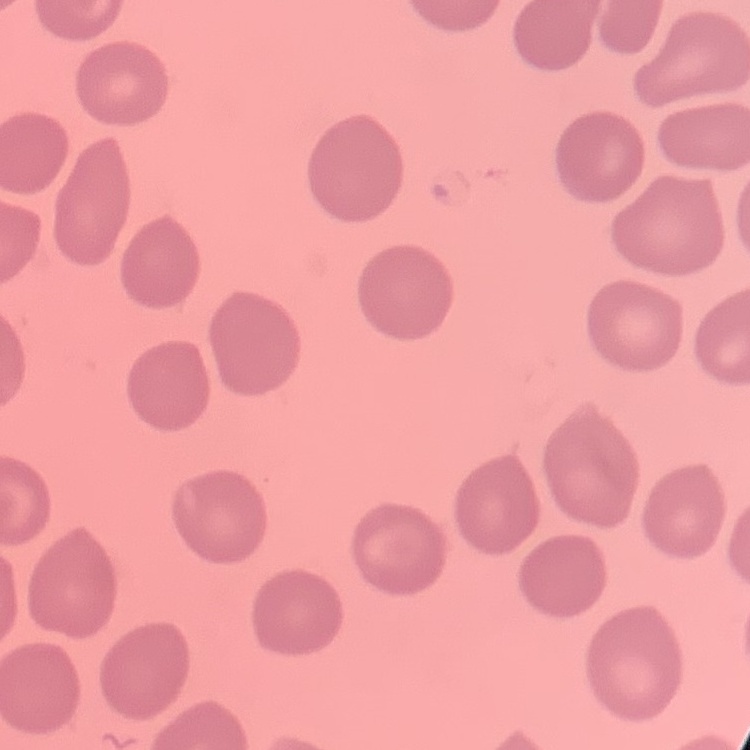
erythrocyte morphology = no rouleaux formation
image type = square crop of a larger photomicrograph
preparation = thin blood film
stain = Field's or Giemsa